Assess this cell for malaria.
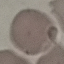

It is uninfected.

Automatically extracted cell patch, resized to 64 × 64 pixels. Giemsa stain. Acquired by smartphone through the microscope eyepiece. Thin blood film.